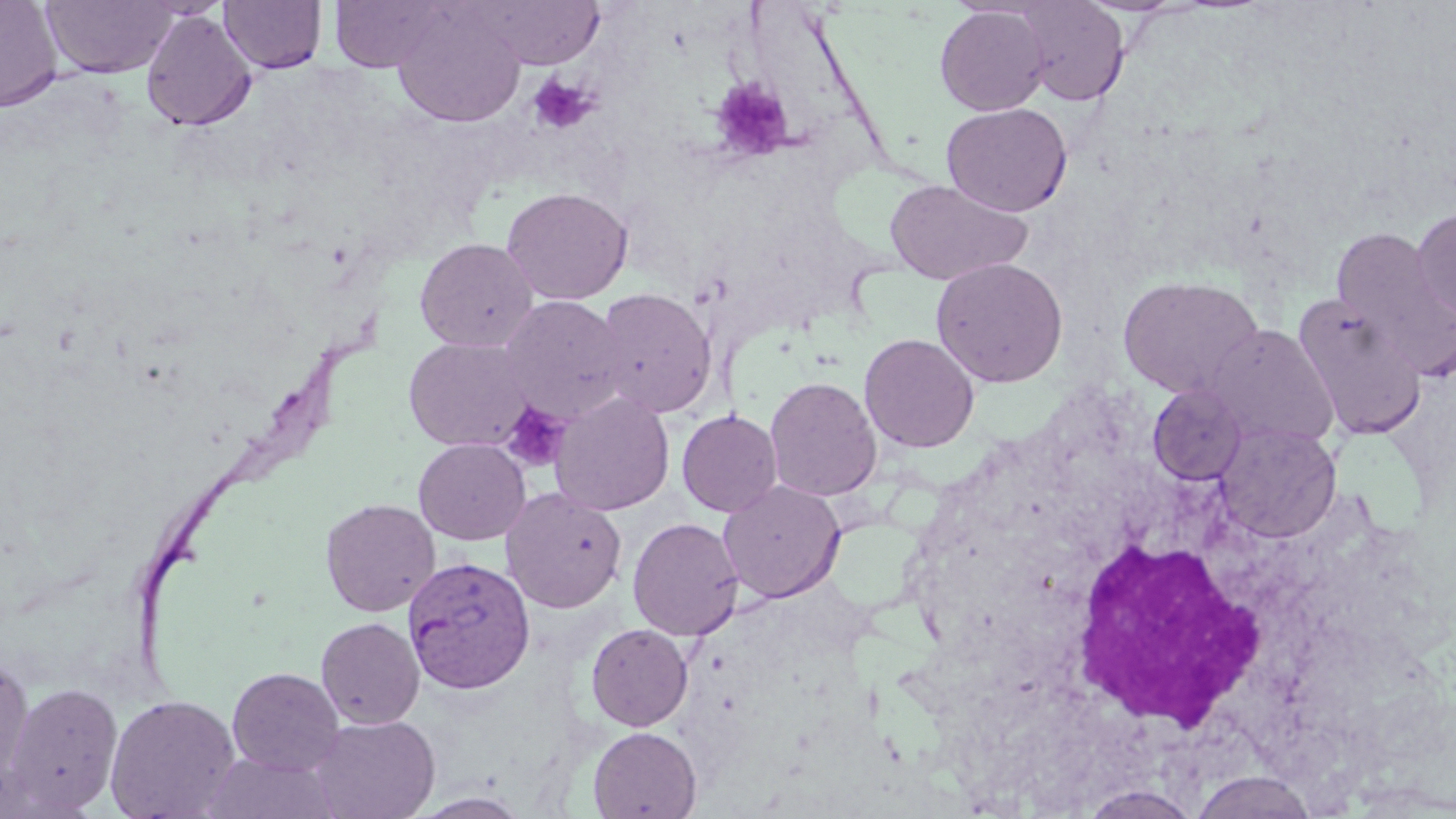
Approximate bounding boxes as named x1/y1/x2/y2 corners in pixels. Platelet locations: (x1=529, y1=73, x2=599, y2=135), (x1=708, y1=77, x2=794, y2=163), (x1=499, y1=399, x2=572, y2=473). White blood cell locations: (x1=1060, y1=535, x2=1274, y2=733). Plasmodium vivax-infected red blood cell locations: (x1=403, y1=556, x2=536, y2=693). Uninfected red blood cell locations: (x1=0, y1=0, x2=63, y2=111), (x1=328, y1=0, x2=453, y2=71), (x1=473, y1=0, x2=605, y2=68), (x1=41, y1=1, x2=178, y2=79), (x1=219, y1=1, x2=327, y2=74), (x1=1012, y1=1, x2=1132, y2=107), (x1=934, y1=5, x2=1050, y2=116), (x1=392, y1=6, x2=526, y2=127), (x1=140, y1=10, x2=257, y2=132), (x1=941, y1=102, x2=1073, y2=216), (x1=885, y1=179, x2=1032, y2=285), (x1=501, y1=186, x2=633, y2=305), (x1=1411, y1=207, x2=1456, y2=325), (x1=1330, y1=224, x2=1452, y2=362), (x1=414, y1=237, x2=539, y2=352), (x1=930, y1=257, x2=1069, y2=388), (x1=1117, y1=275, x2=1265, y2=399), (x1=592, y1=287, x2=718, y2=418), (x1=1291, y1=293, x2=1428, y2=439), (x1=498, y1=295, x2=630, y2=422), (x1=1206, y1=325, x2=1339, y2=450), (x1=859, y1=333, x2=980, y2=453), (x1=403, y1=336, x2=535, y2=452), (x1=765, y1=376, x2=882, y2=502), (x1=1147, y1=384, x2=1247, y2=484), (x1=550, y1=391, x2=675, y2=516), (x1=676, y1=409, x2=783, y2=517), (x1=1217, y1=422, x2=1342, y2=543), (x1=413, y1=438, x2=531, y2=545), (x1=718, y1=480, x2=845, y2=603), (x1=500, y1=487, x2=627, y2=613), (x1=320, y1=498, x2=440, y2=617), (x1=627, y1=517, x2=744, y2=640), (x1=316, y1=617, x2=425, y2=729), (x1=585, y1=623, x2=694, y2=731), (x1=0, y1=658, x2=35, y2=794), (x1=227, y1=667, x2=345, y2=776), (x1=2, y1=681, x2=124, y2=816), (x1=104, y1=694, x2=241, y2=819), (x1=308, y1=714, x2=440, y2=819), (x1=588, y1=726, x2=702, y2=818), (x1=201, y1=751, x2=340, y2=819), (x1=1188, y1=771, x2=1319, y2=818), (x1=1079, y1=784, x2=1205, y2=819), (x1=409, y1=791, x2=533, y2=818). Slide-level diagnosis: Plasmodium vivax. Captured at 1000x magnification. Single field of view. Thin blood film. Light microscopy. May-Grünwald-Giemsa stain. Image is 1456×819 pixels.